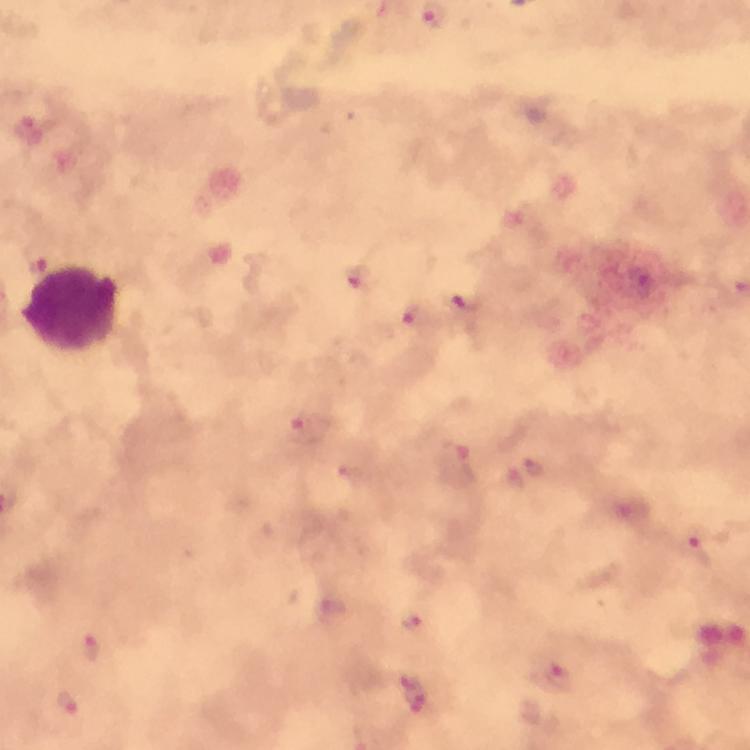
Approximate centers as (x, y) in pixels.
Summary:
  - Plasmodium parasite locations: (29, 134), (354, 276), (474, 303), (415, 310), (308, 426), (455, 466), (535, 471), (509, 476), (352, 477), (697, 547), (331, 604), (408, 614), (90, 649), (546, 664), (420, 688), (68, 701)
  - Leukocyte locations: (77, 309)
  - Magnification: 100x
  - Capture: smartphone camera through the microscope
  - Stain: Giemsa
  - Immersion oil: applied
  - Preparation: thick blood smear
  - Context: from a malaria diagnostic workup
  - Image size: 750×750 pixels
  - Cropped from: a single field of view